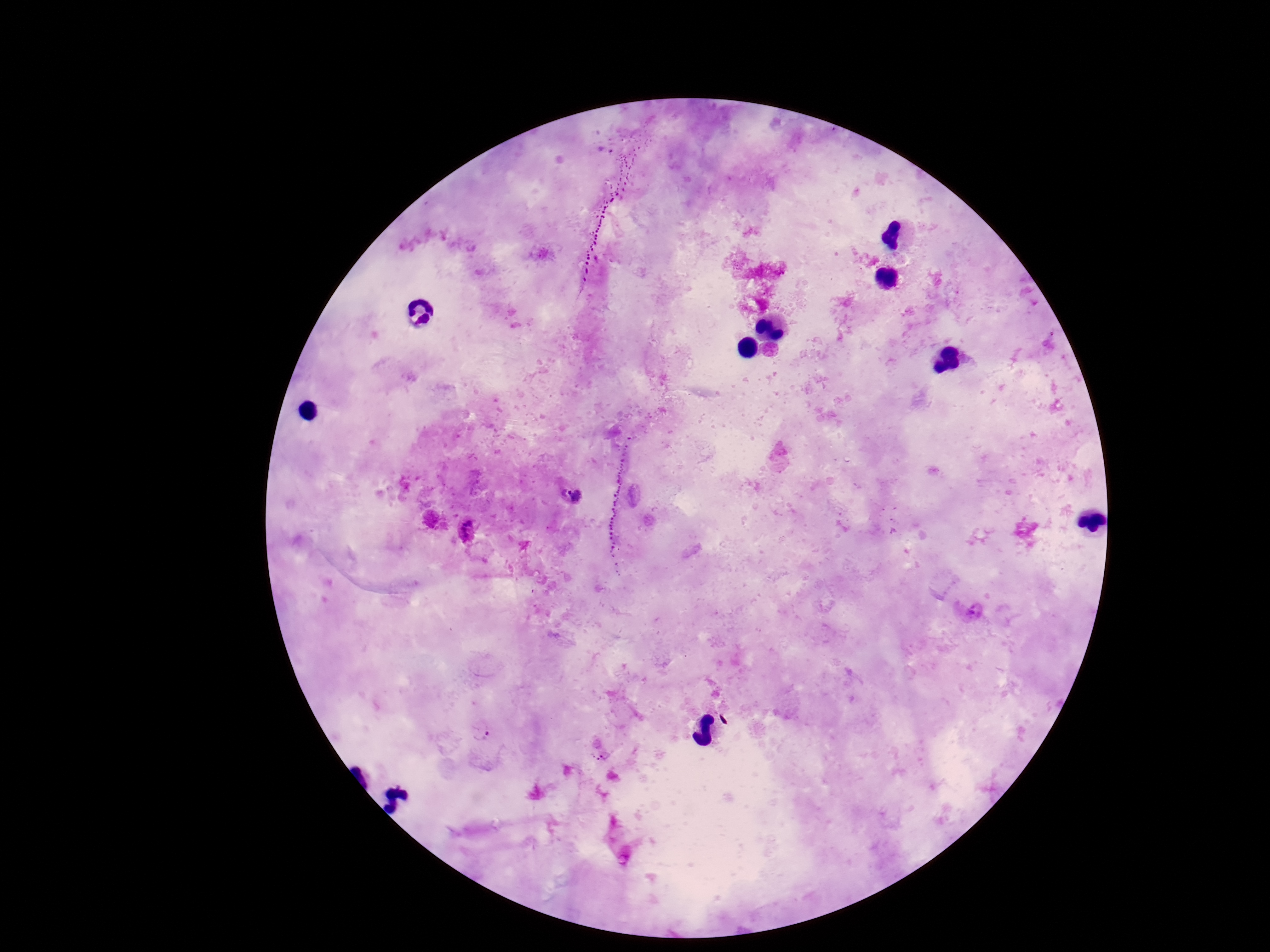 Approximate centers as [x, y] in pixels. Plasmodium parasite locations: [573, 491], [465, 531], [481, 730], [603, 755]. Image is 1270×952 pixels. Giemsa-stained preparation. Thick peripheral-blood smear. One field from this slide. Patient malaria status: positive. 100x magnification. Smartphone photograph taken through the microscope eyepiece.